Locate every white blood cell.
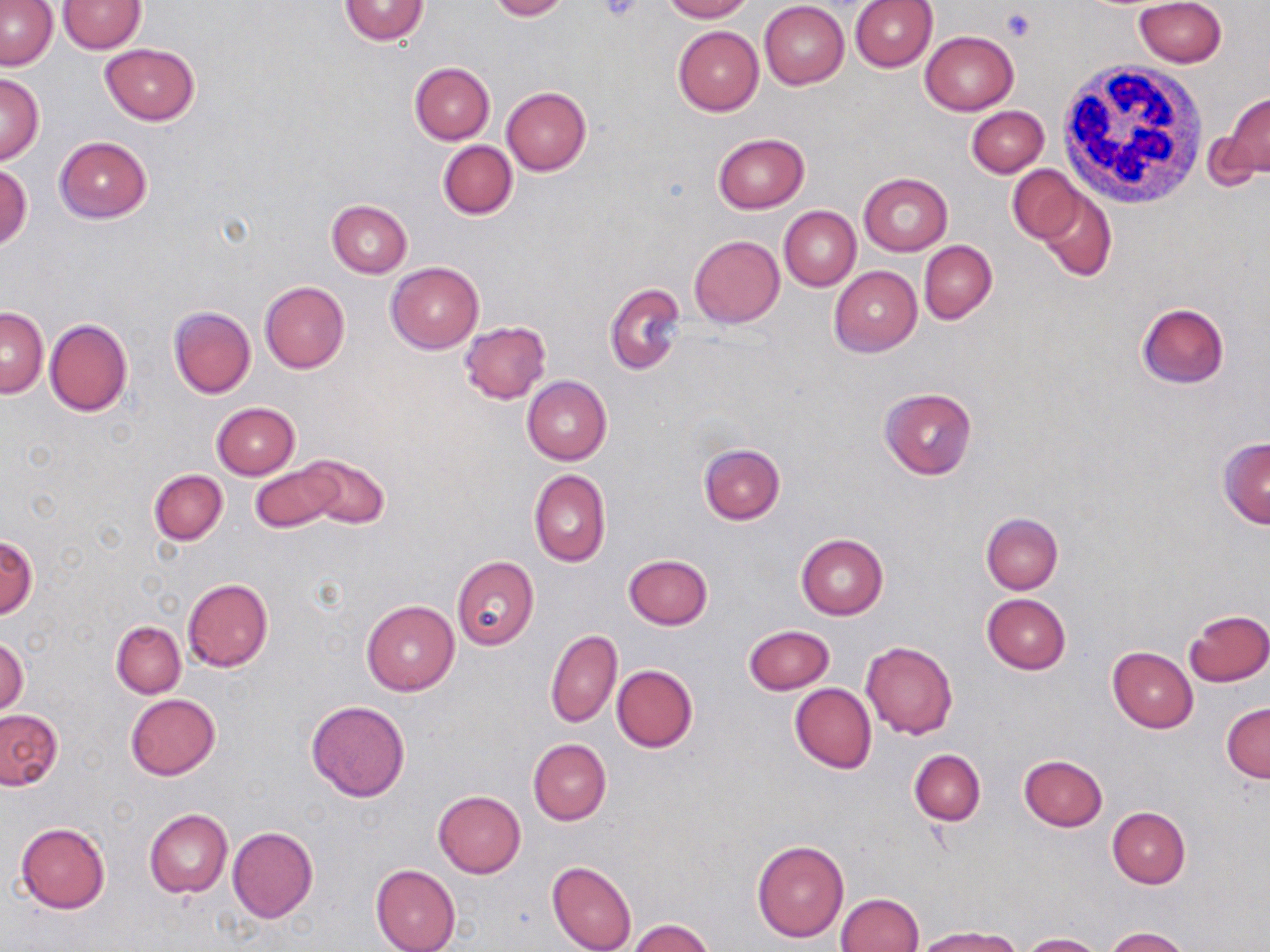
Approximate bounding boxes as (x1,y1)-(x2,y2) corner pairs in pixels.
White blood cells: (1055,62)-(1210,208).

Uninfected red blood cell locations: (340,0)-(430,44), (487,0)-(569,21), (660,0)-(752,22), (1134,0)-(1226,69), (1,1)-(58,71), (59,1)-(145,52), (851,1)-(936,72), (759,2)-(849,89), (673,25)-(763,116), (920,31)-(1018,115), (101,43)-(200,124), (409,62)-(495,144), (0,73)-(44,163), (501,86)-(591,176), (1224,92)-(1269,180), (966,105)-(1048,177), (1204,117)-(1266,198), (713,132)-(808,213), (54,136)-(152,223), (438,141)-(517,219), (1,165)-(31,250), (1007,166)-(1084,243), (858,173)-(952,256), (1033,185)-(1116,282), (326,201)-(411,278), (779,206)-(860,290), (689,235)-(784,327), (919,241)-(996,323), (386,262)-(484,353), (830,266)-(922,357), (604,281)-(685,375), (260,282)-(350,374), (1136,303)-(1229,388), (168,306)-(255,399), (1,307)-(48,398), (44,319)-(132,417), (460,320)-(550,404), (523,376)-(612,465), (879,386)-(978,479), (212,402)-(299,479), (1217,437)-(1270,527), (698,444)-(785,525), (299,454)-(390,529), (250,463)-(343,532), (149,469)-(226,544), (528,469)-(610,568), (981,512)-(1063,593), (1,533)-(37,619), (796,533)-(888,619), (624,555)-(713,629), (452,556)-(539,650), (182,579)-(273,672), (981,593)-(1070,674), (361,600)-(458,695), (1185,609)-(1270,687), (111,621)-(186,698), (742,625)-(835,695), (545,628)-(622,727), (0,637)-(29,716), (861,641)-(958,740), (1108,646)-(1197,732), (612,665)-(698,752), (790,683)-(876,773), (126,693)-(219,780), (306,700)-(410,801), (1222,702)-(1270,783), (0,709)-(63,790), (528,740)-(610,825), (909,750)-(985,825), (1020,754)-(1108,831), (433,791)-(526,878), (1107,807)-(1190,888), (144,809)-(232,897), (15,822)-(110,913), (227,826)-(318,924), (752,840)-(849,943), (547,860)-(636,952), (371,864)-(460,952), (836,893)-(923,952), (627,919)-(715,952), (913,927)-(1018,952), (1104,927)-(1190,952), (1019,932)-(1103,951). Platelet locations: (598,0)-(644,22), (1002,10)-(1035,41). Slide-level diagnosis: negative for blood parasites. Image is 1270×952 pixels. May-Grünwald-Giemsa-stained preparation. 1000x magnification. Single field of view. Optical microscopy. Thin blood smear.